Identify the preparation type.
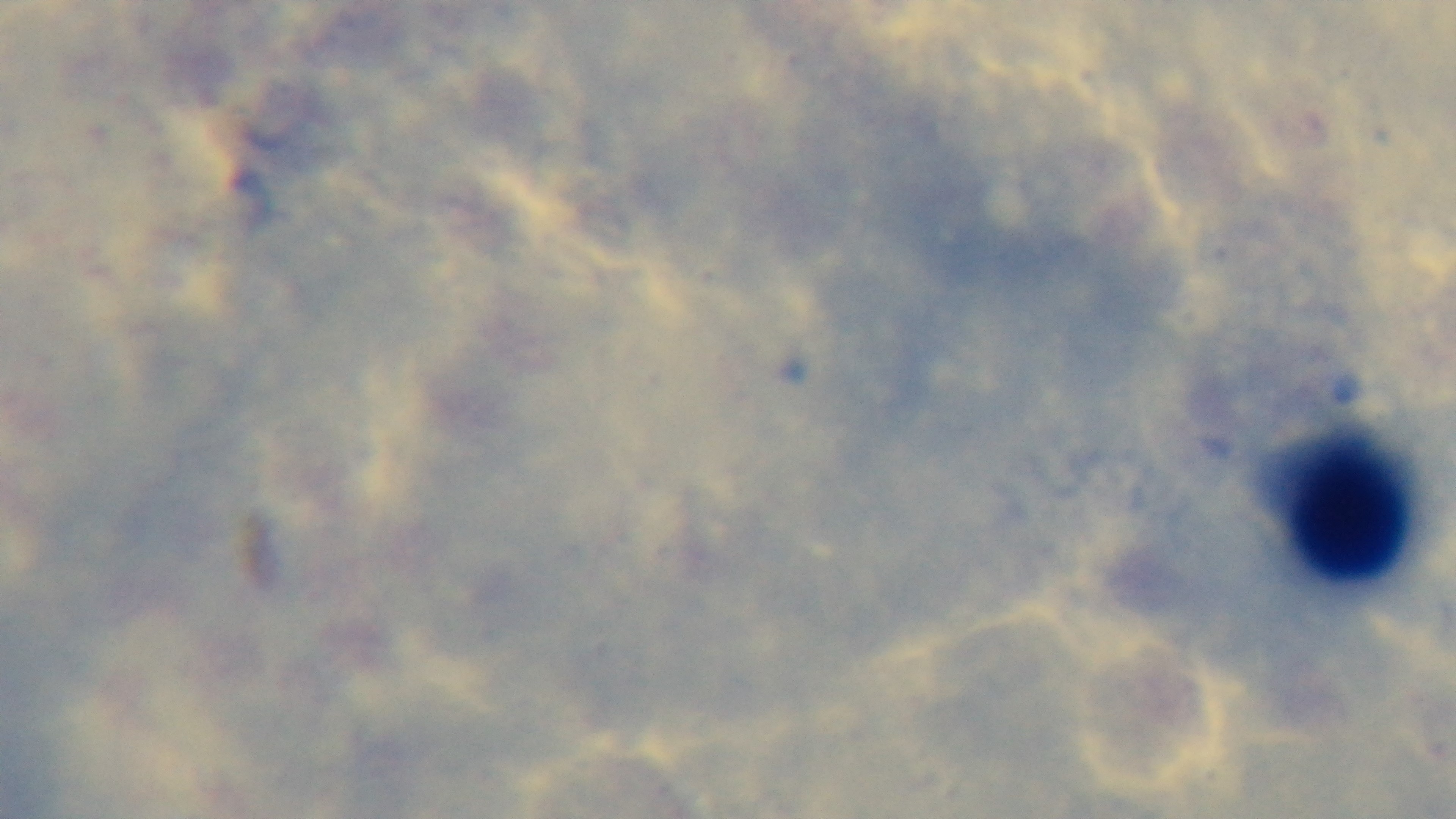

Thick.

Captured with a mounted 4K digital camera. Single field of view. Oil-immersion objective, 100x. Giemsa stain. Malaria status: negative. Light microscopy.